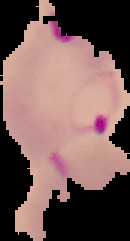 Segmented cell region on a black background. Image is 130×241 pixels. Malaria status: parasitized. From a thin blood smear.